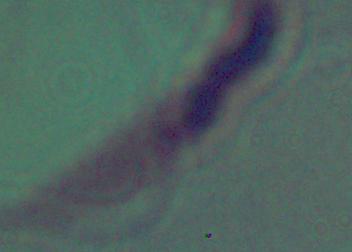
A Leishmania parasite is shown. Micrograph. Captured at 1000x magnification.